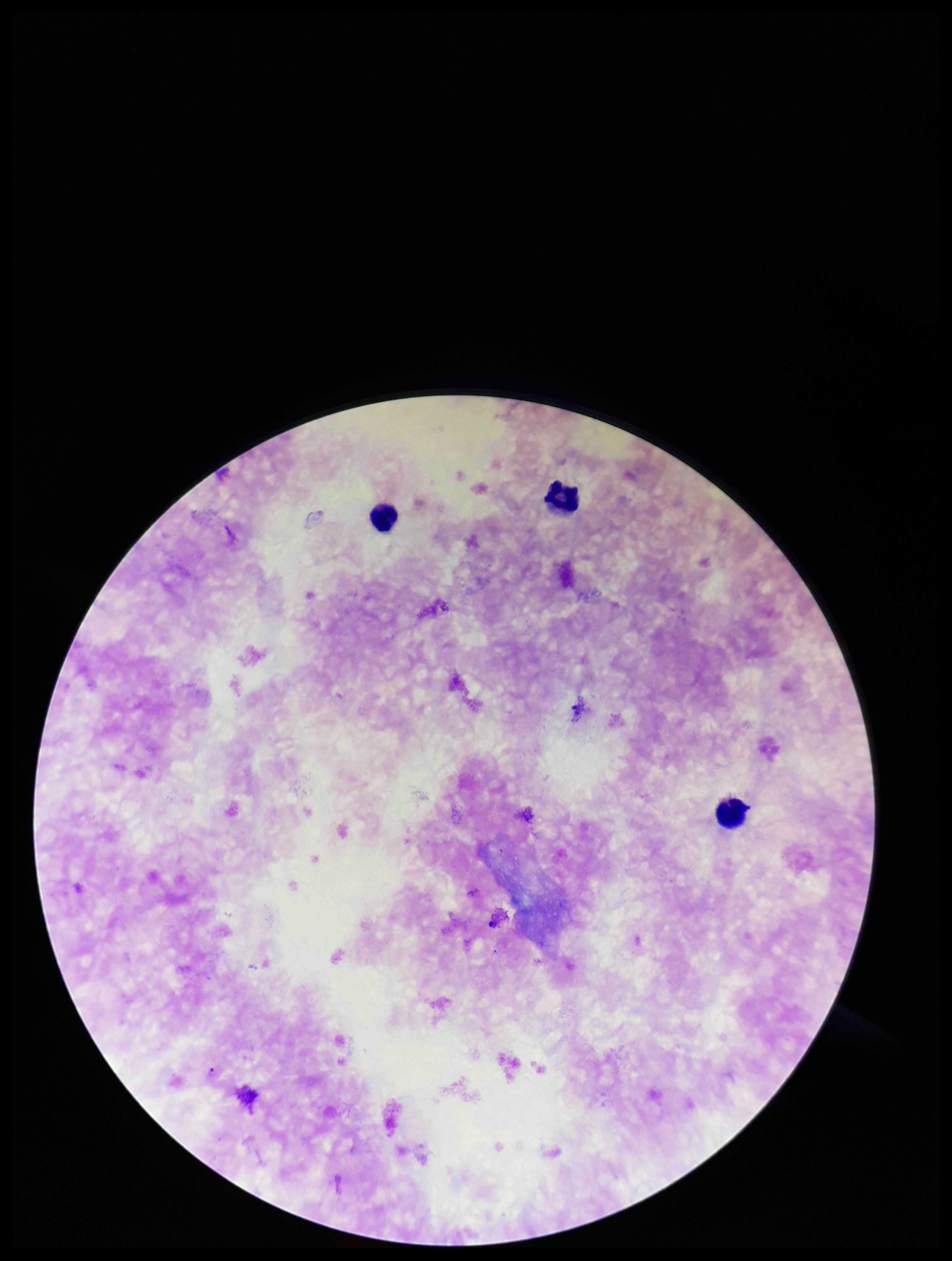
Giemsa stain. Species reported for this patient: Plasmodium falciparum. Image is 952×1261 pixels. Patient malaria status: positive. Parasite count: 1. Leukocyte count: 3. Photographed through the microscope eyepiece with a smartphone camera. Preparation: thick. One field from this slide. Plasmodium parasites: detected.